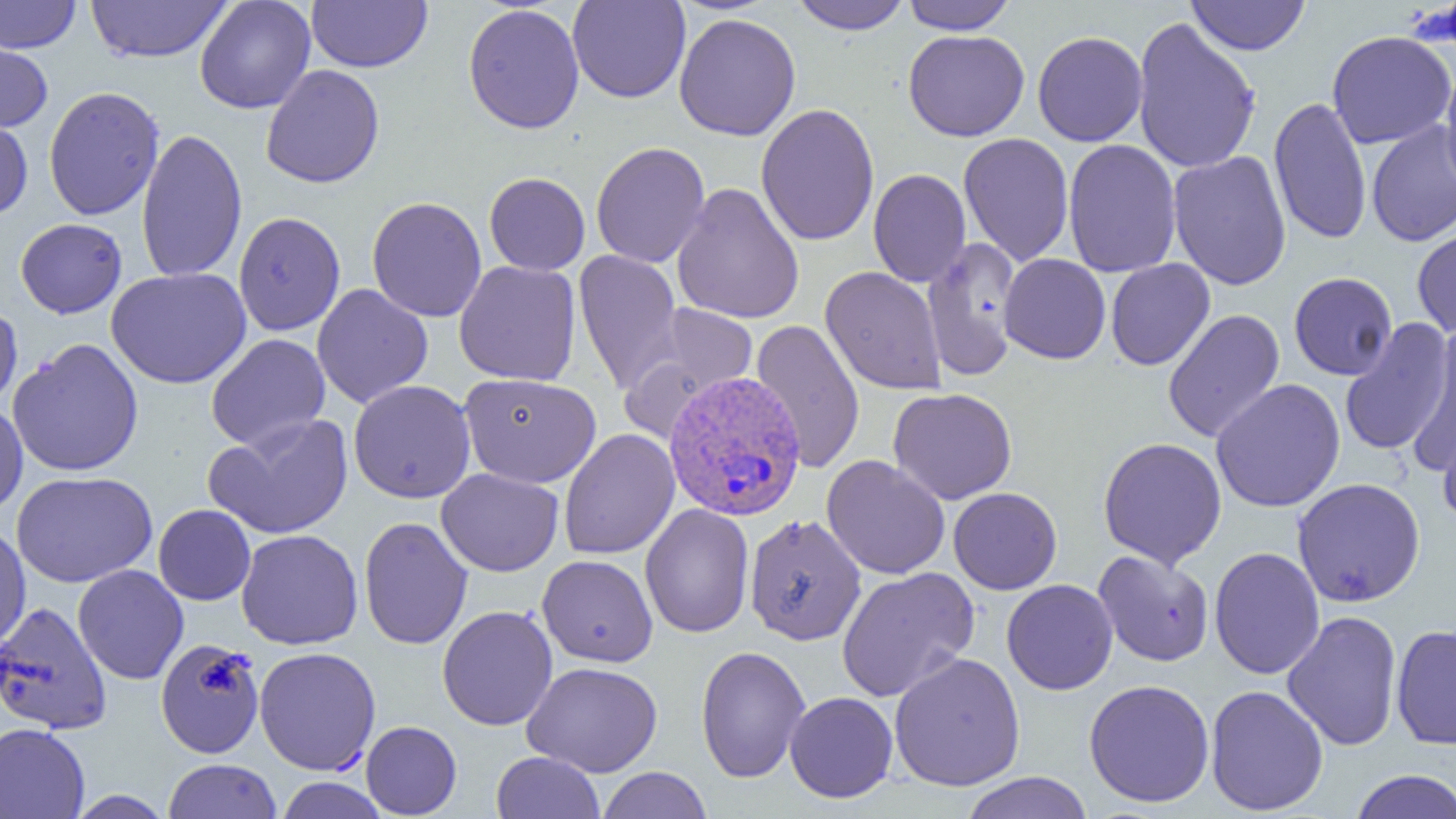

Summary:
  - Coordinate format: approximate bounding boxes as named x1/y1/x2/y2 corners in pixels
  - Uninfected red blood cell locations: (x1=0, y1=0, x2=81, y2=53), (x1=86, y1=0, x2=232, y2=63), (x1=194, y1=0, x2=315, y2=114), (x1=306, y1=0, x2=432, y2=73), (x1=567, y1=0, x2=691, y2=103), (x1=789, y1=0, x2=912, y2=34), (x1=900, y1=0, x2=1019, y2=34), (x1=1186, y1=0, x2=1310, y2=56), (x1=463, y1=4, x2=585, y2=134), (x1=674, y1=13, x2=801, y2=141), (x1=1132, y1=15, x2=1261, y2=175), (x1=903, y1=29, x2=1030, y2=141), (x1=1032, y1=30, x2=1148, y2=147), (x1=1326, y1=30, x2=1455, y2=149), (x1=0, y1=33, x2=53, y2=132), (x1=260, y1=65, x2=385, y2=189), (x1=1439, y1=66, x2=1456, y2=197), (x1=43, y1=86, x2=164, y2=221), (x1=1269, y1=96, x2=1371, y2=246), (x1=756, y1=103, x2=880, y2=247), (x1=0, y1=112, x2=33, y2=220), (x1=1366, y1=121, x2=1456, y2=247), (x1=136, y1=127, x2=247, y2=283), (x1=958, y1=132, x2=1074, y2=266), (x1=1063, y1=139, x2=1181, y2=278), (x1=591, y1=141, x2=711, y2=269), (x1=1168, y1=150, x2=1291, y2=291), (x1=868, y1=169, x2=972, y2=287), (x1=484, y1=172, x2=590, y2=275), (x1=671, y1=182, x2=805, y2=325), (x1=367, y1=196, x2=487, y2=322), (x1=233, y1=211, x2=346, y2=336), (x1=15, y1=218, x2=127, y2=318), (x1=1412, y1=221, x2=1456, y2=340), (x1=922, y1=237, x2=1024, y2=380), (x1=574, y1=249, x2=683, y2=395), (x1=999, y1=254, x2=1111, y2=364), (x1=1105, y1=258, x2=1215, y2=371), (x1=454, y1=260, x2=581, y2=386), (x1=821, y1=266, x2=946, y2=396), (x1=106, y1=267, x2=251, y2=389), (x1=1288, y1=272, x2=1398, y2=380), (x1=312, y1=284, x2=433, y2=408), (x1=0, y1=302, x2=23, y2=414), (x1=643, y1=303, x2=759, y2=405), (x1=1162, y1=309, x2=1285, y2=443), (x1=750, y1=318, x2=865, y2=474), (x1=1339, y1=319, x2=1454, y2=456), (x1=1408, y1=328, x2=1456, y2=473), (x1=206, y1=333, x2=331, y2=452), (x1=8, y1=338, x2=144, y2=477), (x1=460, y1=372, x2=602, y2=488), (x1=1210, y1=378, x2=1346, y2=513), (x1=348, y1=380, x2=476, y2=503), (x1=888, y1=388, x2=1017, y2=504), (x1=0, y1=402, x2=28, y2=517), (x1=205, y1=413, x2=353, y2=540), (x1=1439, y1=413, x2=1456, y2=529), (x1=558, y1=429, x2=679, y2=559), (x1=1098, y1=437, x2=1227, y2=569), (x1=822, y1=455, x2=950, y2=579), (x1=436, y1=468, x2=564, y2=576), (x1=11, y1=471, x2=157, y2=587), (x1=1292, y1=477, x2=1426, y2=607), (x1=948, y1=487, x2=1062, y2=594), (x1=153, y1=504, x2=256, y2=606), (x1=640, y1=504, x2=754, y2=638), (x1=744, y1=514, x2=867, y2=646), (x1=359, y1=516, x2=473, y2=650), (x1=0, y1=520, x2=30, y2=651), (x1=236, y1=529, x2=363, y2=650), (x1=1209, y1=546, x2=1325, y2=680), (x1=1093, y1=550, x2=1214, y2=667), (x1=537, y1=554, x2=658, y2=667), (x1=73, y1=564, x2=189, y2=684), (x1=836, y1=567, x2=979, y2=702), (x1=1001, y1=579, x2=1118, y2=695), (x1=0, y1=601, x2=112, y2=735), (x1=437, y1=605, x2=558, y2=730), (x1=1281, y1=610, x2=1402, y2=751), (x1=1391, y1=624, x2=1456, y2=749), (x1=155, y1=637, x2=265, y2=759), (x1=695, y1=645, x2=810, y2=783), (x1=254, y1=646, x2=381, y2=775), (x1=889, y1=652, x2=1026, y2=792), (x1=523, y1=661, x2=663, y2=777), (x1=1084, y1=679, x2=1215, y2=807), (x1=1205, y1=684, x2=1329, y2=816), (x1=785, y1=691, x2=898, y2=803), (x1=361, y1=721, x2=461, y2=818), (x1=0, y1=723, x2=90, y2=818), (x1=491, y1=751, x2=605, y2=818), (x1=162, y1=759, x2=282, y2=818), (x1=596, y1=767, x2=712, y2=818), (x1=1349, y1=769, x2=1456, y2=819), (x1=959, y1=771, x2=1093, y2=819), (x1=274, y1=777, x2=388, y2=818), (x1=66, y1=790, x2=174, y2=819)
  - Plasmodium vivax-infected red blood cell locations: (x1=662, y1=369, x2=807, y2=521)
  - Slide-level diagnosis: Plasmodium vivax
  - Field of view: one of a larger specimen
  - Preparation: thin blood smear
  - Image size: 1456×819 pixels
  - Modality: light microscopy
  - Magnification: 1000x